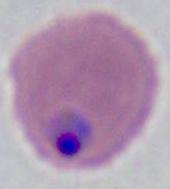

A Plasmodium parasite is seen. Captured at either 400x or 1000x magnification. Photomicrograph.